Comment on the morphology of the erythrocytes.
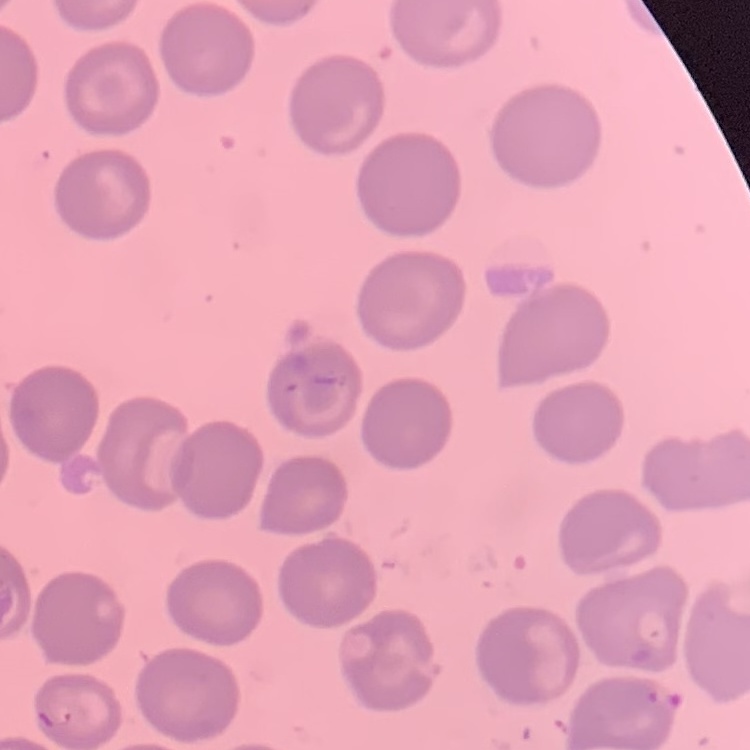
No rouleaux formation.

preparation: thin peripheral smear
image_type: square crop of a larger photomicrograph
stain: Field's or Giemsa